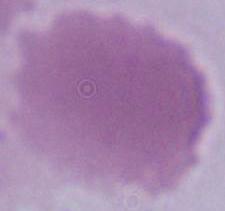
Micrograph. Captured at 1000x magnification. An erythrocyte is shown.